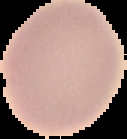

{
  "image_type": "cell region segmented out of the field of view; surrounding area masked to black",
  "image_size": "127×139 pixels",
  "malaria_status": "uninfected",
  "preparation": "thin blood smear"
}